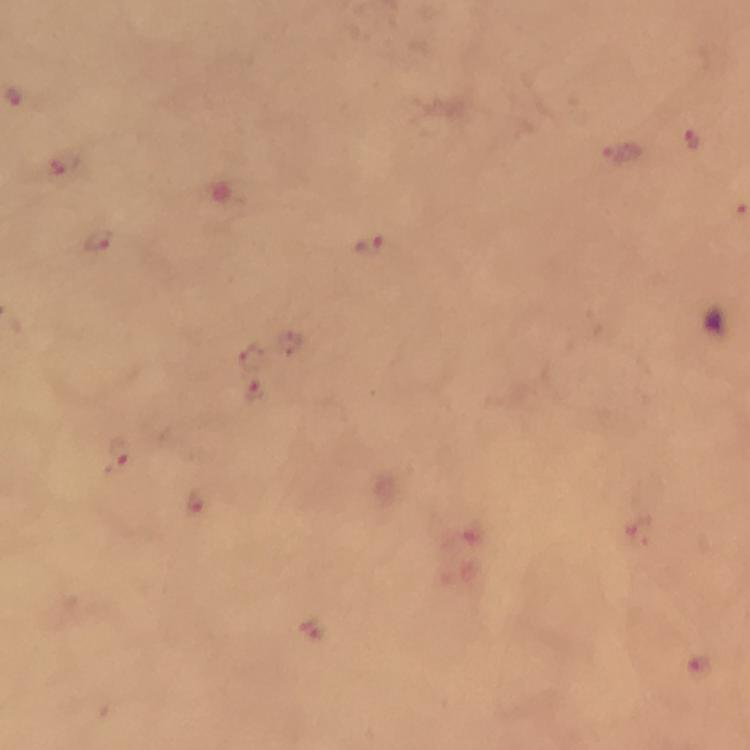

stain = Giemsa
context = from a malaria diagnostic workup
Plasmodium parasite locations = approximate object centers, in pixels from the top-left corner: (x=692, y=141), (x=618, y=154), (x=63, y=164), (x=95, y=240), (x=369, y=247), (x=295, y=342), (x=251, y=357), (x=255, y=392), (x=120, y=454), (x=197, y=504), (x=311, y=629)
preparation = thick blood film
image size = 750×750 pixels
immersion oil = used
cropped from = one field of view
magnification = 100x
capture = smartphone mounted on the microscope